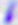
Summary:
  - Modality: micrograph
  - Identification: Toxoplasma gondii
  - Magnification: 400x